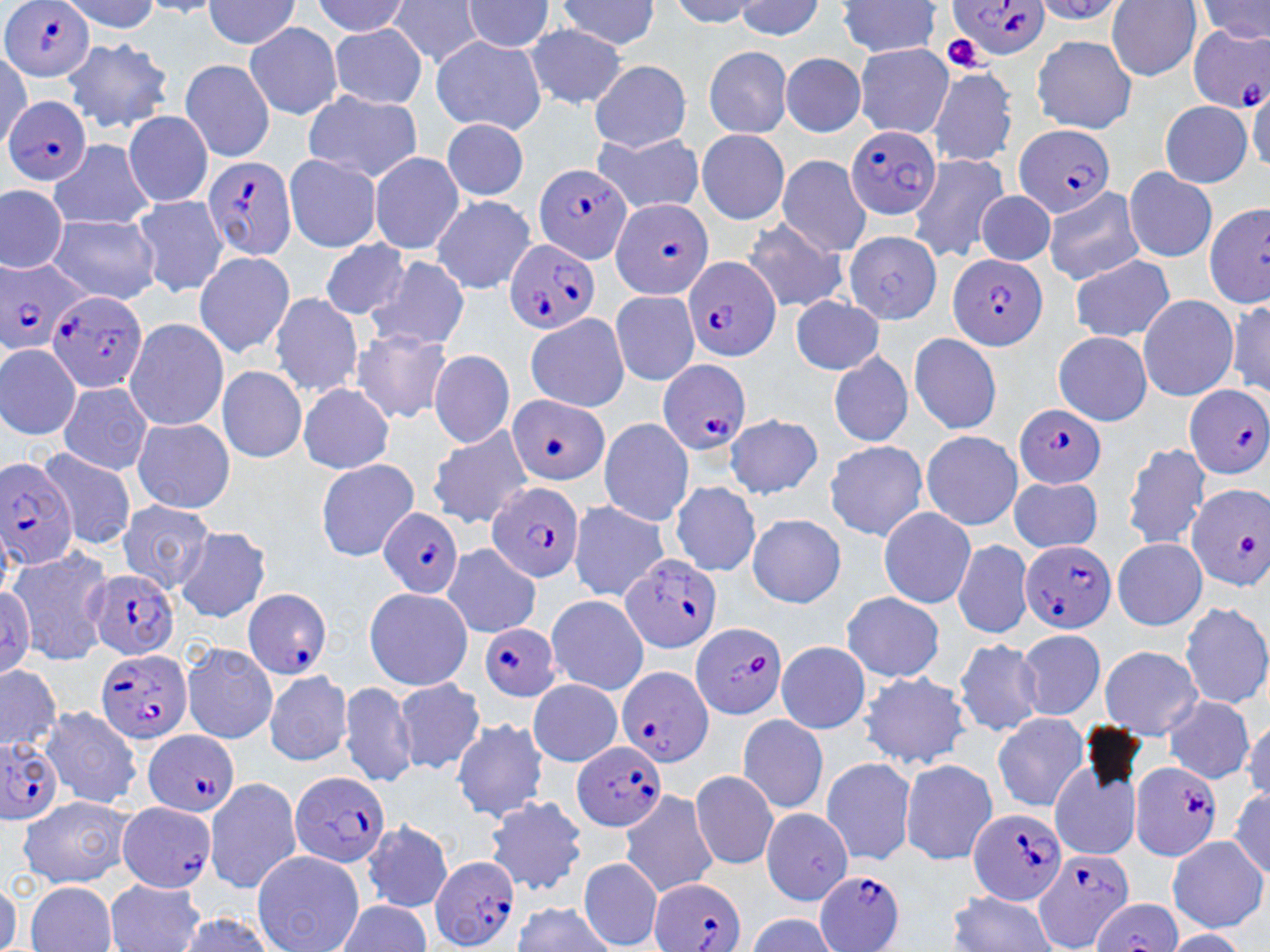

Approximate bounding boxes as (x1,y1)-(x2,y2) corner pairs in pixels. Uninfected red blood cell locations (subset): (382,0)-(481,68), (553,0)-(668,50), (1109,0)-(1198,79), (738,1)-(823,40), (464,2)-(552,54), (839,3)-(947,57), (205,5)-(301,52), (520,21)-(634,110), (245,24)-(345,120), (330,24)-(426,107), (1029,33)-(1137,129), (430,37)-(550,135), (63,39)-(170,134), (854,43)-(954,142), (700,47)-(799,144), (778,54)-(866,138), (180,59)-(273,165), (587,62)-(690,153), (705,85)-(791,134), (783,85)-(864,136), (858,85)-(954,134), (926,86)-(1018,164), (300,89)-(423,183), (1157,98)-(1253,183), (121,111)-(215,207), (437,118)-(532,200), (696,125)-(789,227), (591,137)-(707,211), (370,149)-(463,253), (285,150)-(383,252), (913,156)-(1013,262), (41,157)-(160,231), (776,158)-(872,256), (1124,165)-(1217,262), (0,186)-(71,274), (1046,187)-(1150,284), (975,190)-(1063,268), (139,194)-(226,295), (429,195)-(536,292), (1203,203)-(1270,309), (739,219)-(852,314), (46,220)-(162,303), (846,229)-(941,324), (318,236)-(409,319), (193,252)-(294,358), (1066,255)-(1174,343), (366,256)-(477,351), (607,290)-(704,389), (272,292)-(366,398), (792,295)-(885,378), (1139,295)-(1238,404), (523,313)-(630,414), (124,320)-(228,430), (348,326)-(454,423), (906,330)-(1001,430), (1050,333)-(1157,432), (0,344)-(80,439), (825,350)-(913,448), (432,351)-(514,446), (221,369)-(307,464), (300,384)-(393,476), (59,385)-(153,477), (724,410)-(825,496), (599,419)-(696,526), (135,422)-(233,511), (426,423)-(534,527), (921,427)-(1026,530), (821,439)-(930,542), (1121,443)-(1216,550), (42,446)-(141,548), (320,458)-(417,559), (1004,477)-(1104,557), (671,481)-(760,578), (568,499)-(665,604), (119,500)-(217,592), (878,507)-(981,607), (745,509)-(845,611), (179,526)-(275,620), (1111,538)-(1210,627), (948,539)-(1037,642), (10,541)-(118,663), (446,545)-(542,637), (361,587)-(465,687), (837,591)-(950,684), (548,595)-(652,698), (1183,603)-(1268,709), (1010,627)-(1105,719), (773,637)-(868,735), (954,637)-(1048,742), (184,639)-(276,741), (1100,645)-(1203,723), (0,663)-(63,755), (263,666)-(349,766), (854,669)-(971,772), (397,678)-(486,773), (531,681)-(623,764), (338,684)-(417,787), (1161,697)-(1253,785), (44,705)-(143,810), (996,710)-(1088,812), (734,712)-(830,812), (453,719)-(549,823), (903,755)-(1001,865), (820,758)-(915,865), (688,767)-(786,868), (221,779)-(301,895), (1049,782)-(1141,857), (621,793)-(728,895), (19,795)-(134,888), (489,798)-(585,894), (763,803)-(853,904), (364,826)-(456,908), (1167,832)-(1266,934), (249,850)-(366,944), (579,861)-(666,945), (106,880)-(206,942), (28,883)-(113,943), (945,891)-(1056,950), (1093,900)-(1186,952). Plasmodium falciparum-infected red blood cell locations: (948,0)-(1048,63), (0,1)-(95,84), (1186,25)-(1270,113), (2,98)-(96,188), (1012,122)-(1119,219), (847,126)-(947,216), (200,156)-(298,264), (534,158)-(632,261), (609,196)-(714,299), (504,240)-(602,333), (681,254)-(783,364), (949,254)-(1052,348), (0,260)-(97,353), (50,293)-(150,391), (656,358)-(751,455), (1182,382)-(1270,480), (510,389)-(607,485), (1016,404)-(1106,484), (0,454)-(76,567), (1193,482)-(1270,590), (489,483)-(586,582), (378,504)-(460,597), (1022,539)-(1118,632), (614,556)-(724,655), (84,566)-(181,661), (241,584)-(335,673), (692,620)-(789,716), (481,623)-(561,699), (94,645)-(193,743), (616,663)-(716,766), (140,727)-(235,816), (567,735)-(669,835), (1,740)-(61,825), (1127,756)-(1225,863), (289,767)-(391,868), (115,798)-(217,895), (966,806)-(1068,903), (1029,850)-(1132,950), (430,855)-(518,952), (814,870)-(903,950), (650,878)-(750,952). Platelet locations: (941,34)-(996,80). Slide-level diagnosis: Plasmodium falciparum. 1000x magnification. Thin blood smear. Image is 1270×952 pixels. May-Grünwald-Giemsa-stained preparation. One field of a larger specimen. Optical microscopy.